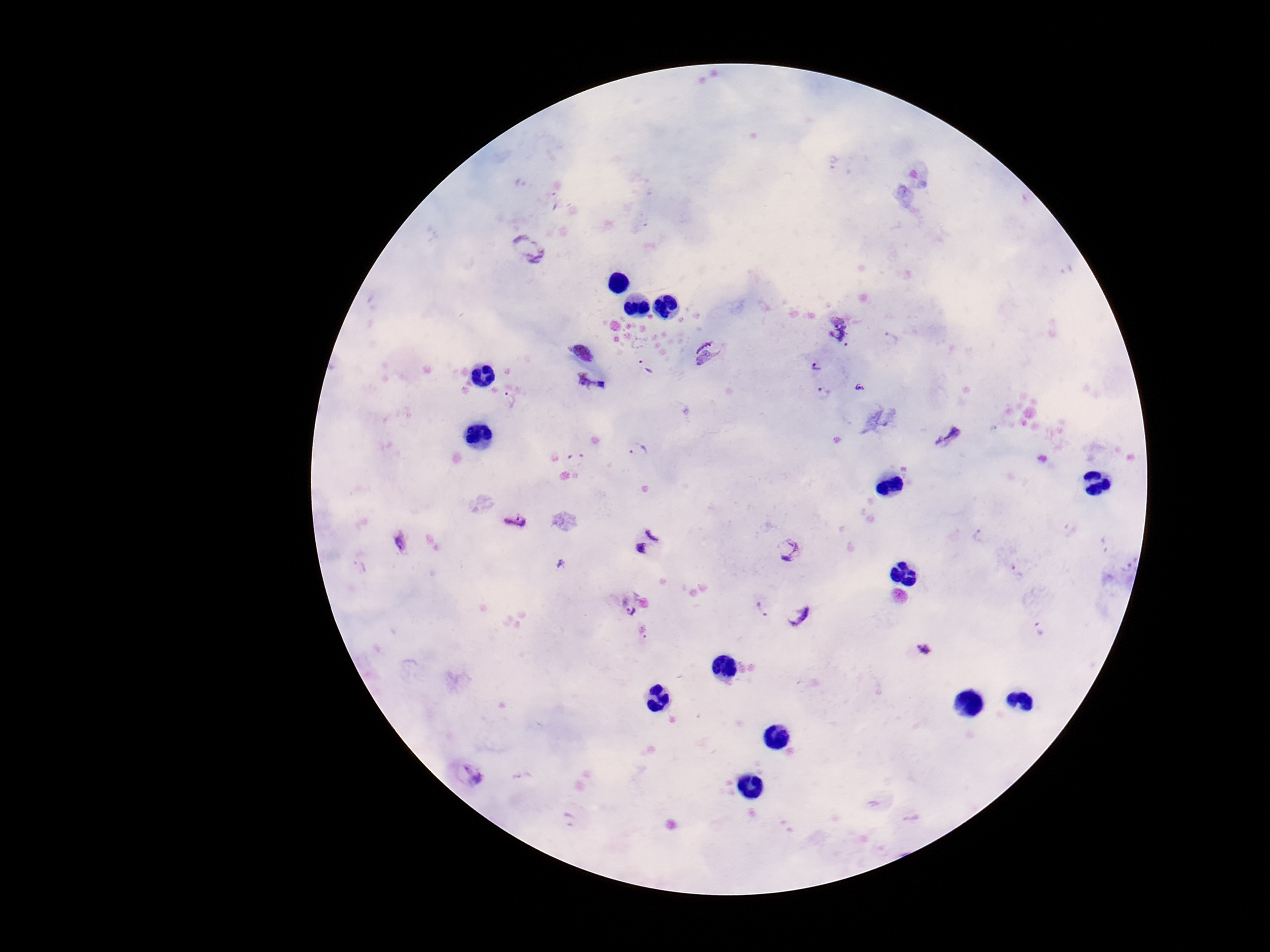
Approximate centers as (x, y) in pixels. Plasmodium parasite locations: (528, 250), (837, 329), (584, 351), (711, 352), (645, 366), (817, 366), (593, 384), (860, 388), (824, 394), (510, 399), (949, 435), (639, 450), (515, 519), (979, 537), (402, 540), (647, 542), (791, 551), (1016, 571), (630, 603), (760, 609), (795, 617), (1038, 628), (644, 633), (924, 650), (469, 775). Smartphone photograph taken through the microscope eyepiece. Single field of view. Image is 1270×952 pixels. 100x magnification. Giemsa stain. Patient malaria status: infected. Thick peripheral-blood smear.